Report the malaria status.
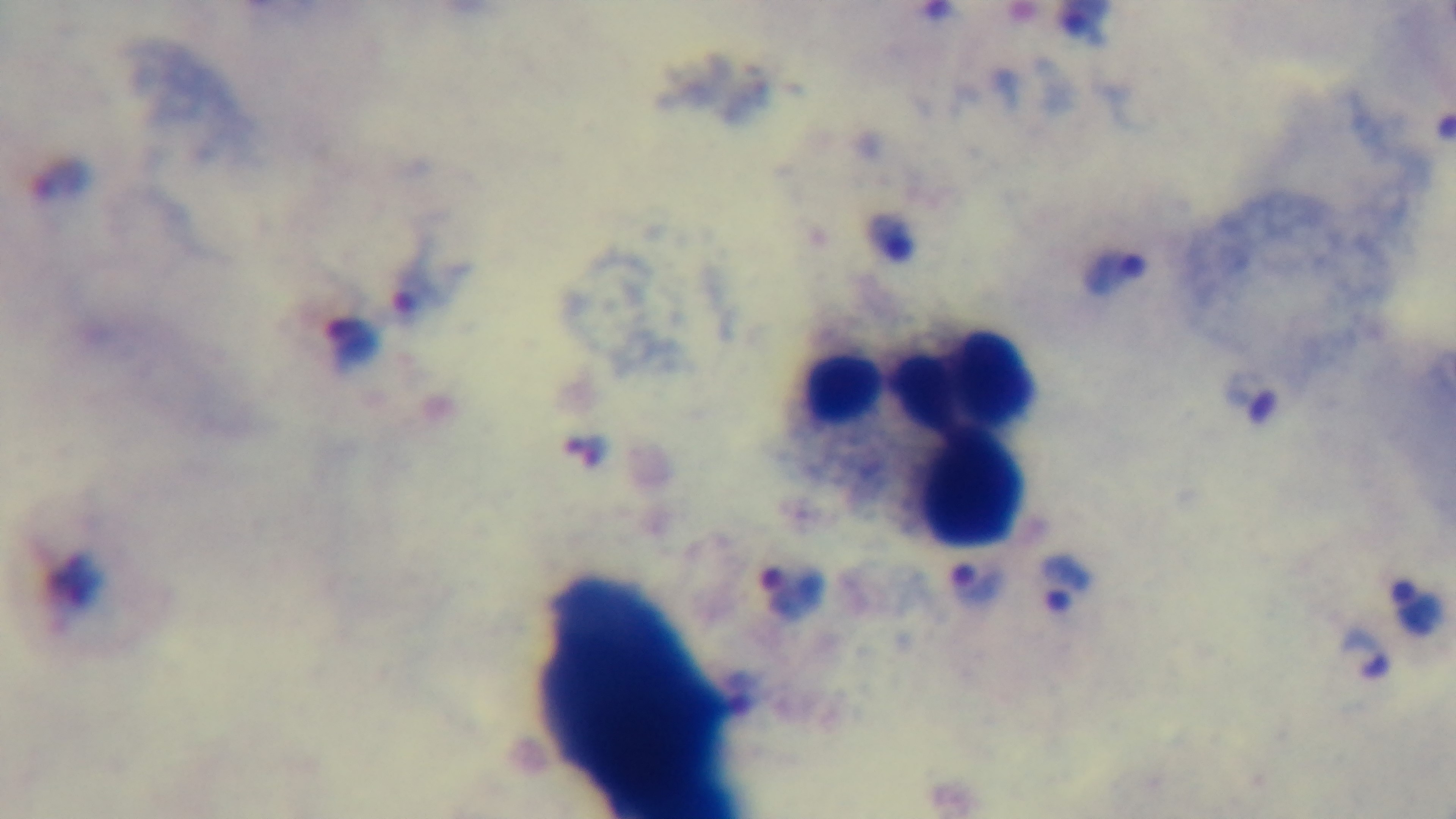
Positive.

preparation = thick
stain = Giemsa
objective = 100x oil immersion
field of view = single
capture = mounted 4K digital camera
modality = light microscopy